Assess for malaria.
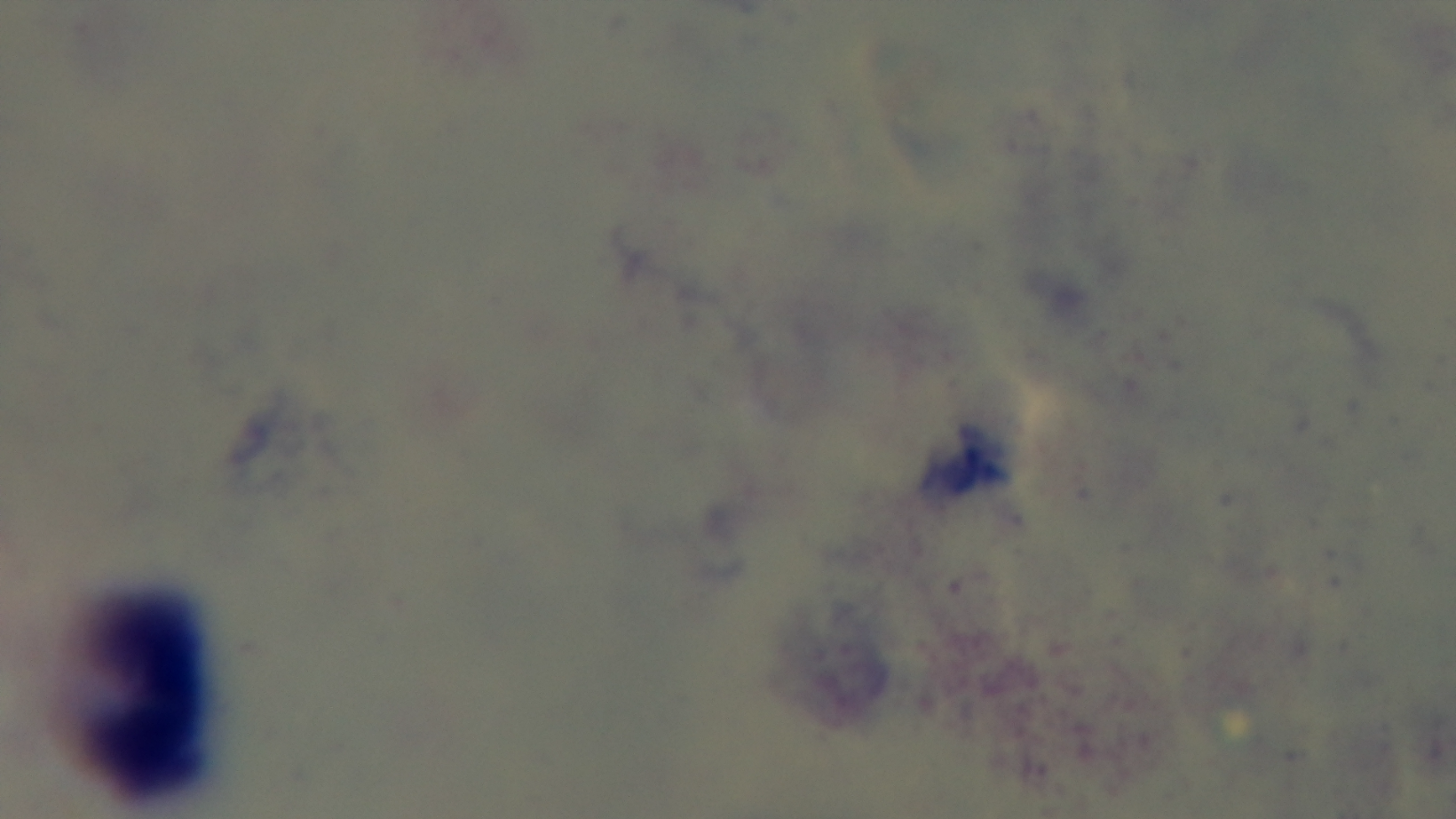
Negative.

modality: light microscopy
objective: 100x oil immersion
field_of_view: one from the slide
stain: Giemsa
capture: mounted 4K digital camera
preparation: thick blood film